Describe the morphology of the erythrocytes.
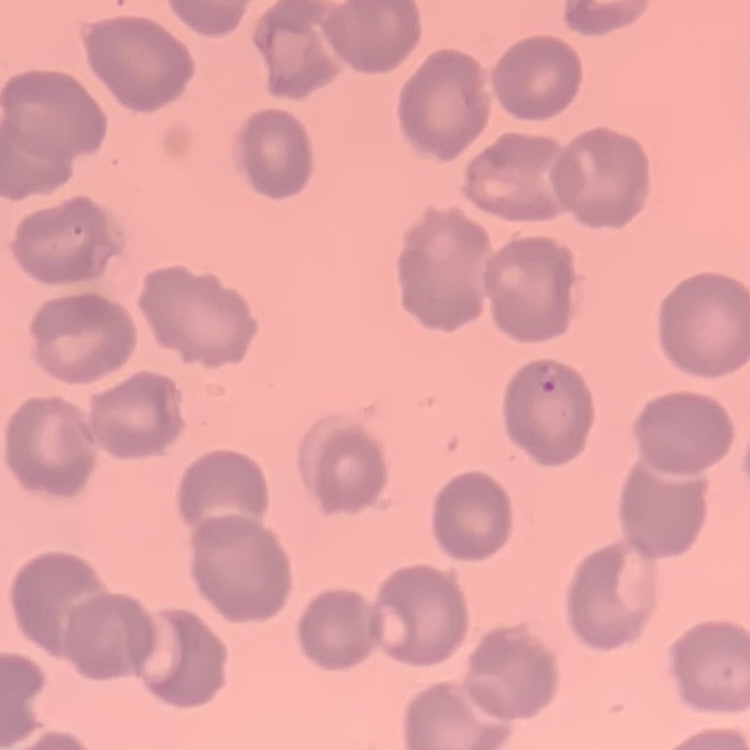

They show no rouleaux formation.

Summary:
  - Preparation: thin blood film
  - Image type: square crop of a larger photomicrograph
  - Stain: Field's or Giemsa